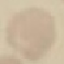

Malaria status: uninfected. Giemsa-stained preparation. Thin smear of blood. Cell patch, automatically extracted from a larger field of view and resized to 64 × 64 pixels. Acquired by smartphone through the microscope eyepiece.